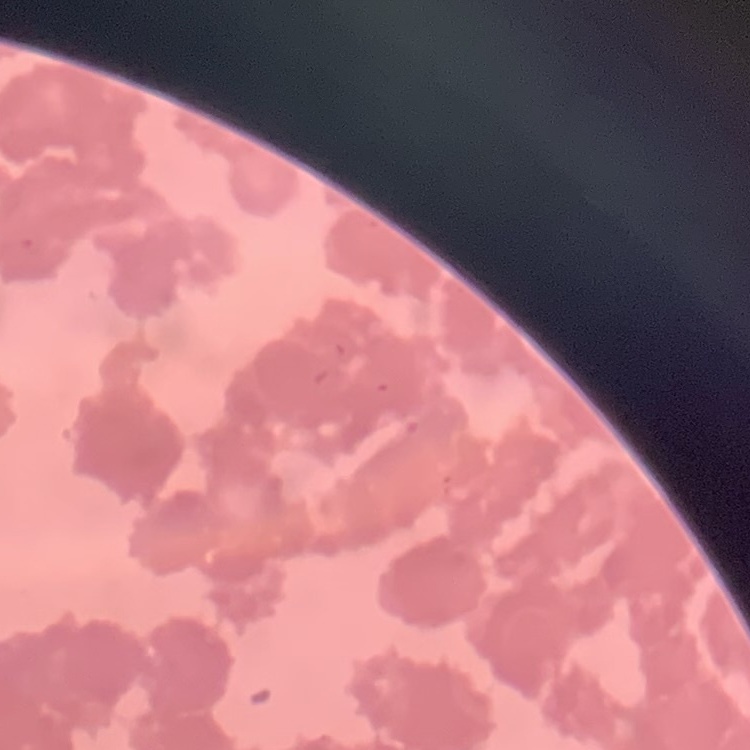

Summary:
  - Erythrocyte morphology: rouleaux formation
  - Preparation: thin blood smear
  - Image type: one tile cut from a larger photomicrograph
  - Stain: Field's or Giemsa